Locate every malaria parasite and every leukocyte.
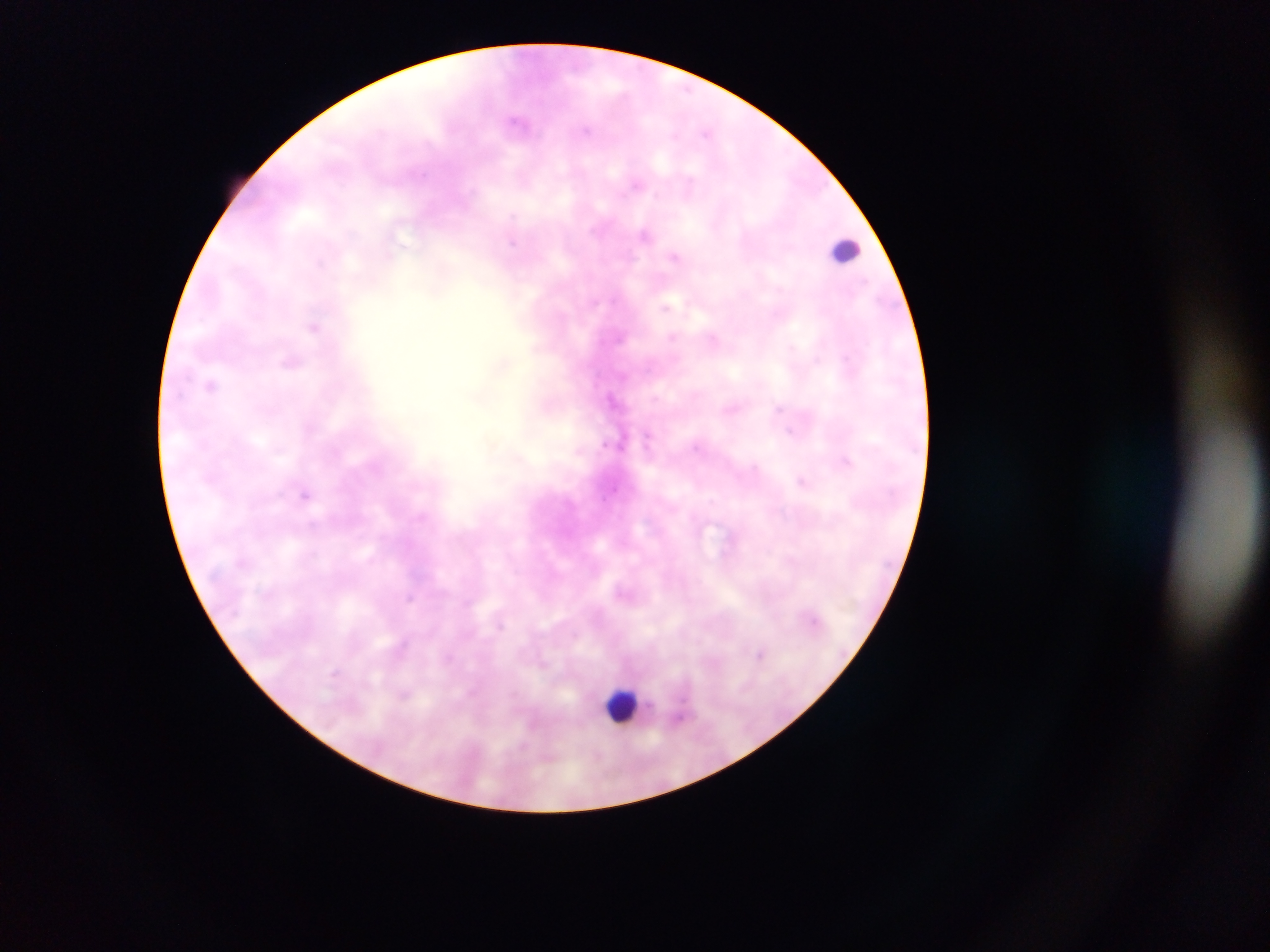

Approximate centers as {x, y} in pixels.
Malaria parasites: {517, 122}, {587, 130}, {707, 132}, {636, 185}, {644, 234}, {388, 255}, {674, 256}, {318, 262}, {667, 307}, {314, 327}, {673, 337}, {713, 339}, {791, 347}, {816, 359}, {290, 362}, {211, 384}, {611, 397}, {778, 408}, {790, 431}, {648, 438}, {846, 461}, {801, 480}, {304, 495}, {410, 598}, {760, 653}, {335, 672}, {405, 695}.
Leukocytes: {844, 248}, {623, 706}.

One field of view. Thick blood smear. Image is 1270×952 pixels. Sample from Ghana. Mobile-phone photograph taken through the microscope.